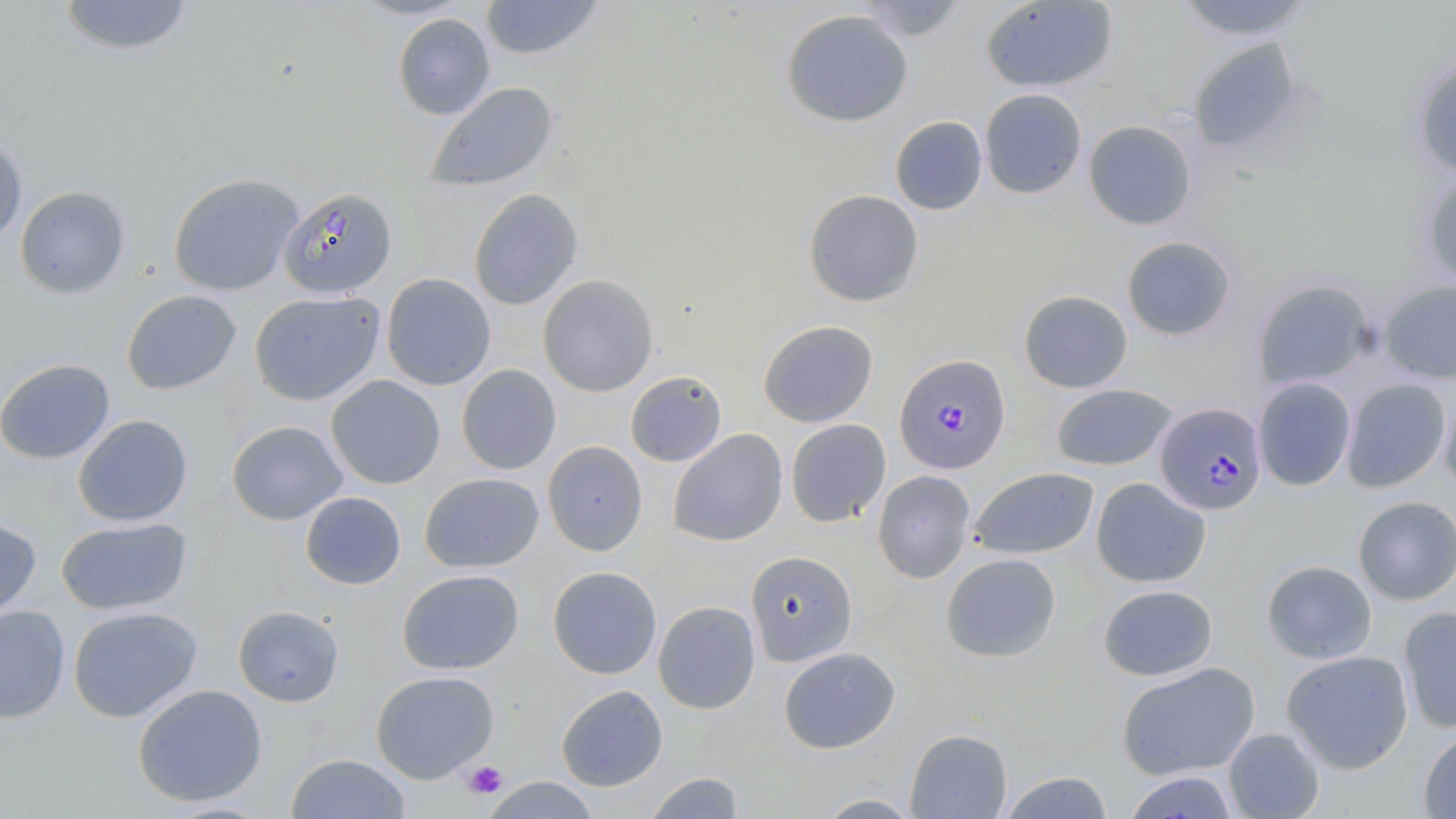

Approximate bounding boxes as named x1/y1/x2/y2 corners in pixels. Platelet locations: (x1=463, y1=760, x2=507, y2=798). Uninfected red blood cell locations: (x1=56, y1=0, x2=195, y2=57), (x1=479, y1=0, x2=606, y2=60), (x1=853, y1=0, x2=968, y2=42), (x1=1173, y1=0, x2=1314, y2=40), (x1=981, y1=1, x2=1118, y2=92), (x1=781, y1=9, x2=913, y2=127), (x1=392, y1=13, x2=495, y2=120), (x1=1188, y1=38, x2=1301, y2=153), (x1=1411, y1=59, x2=1456, y2=180), (x1=425, y1=82, x2=559, y2=192), (x1=979, y1=88, x2=1087, y2=199), (x1=889, y1=116, x2=987, y2=214), (x1=1083, y1=120, x2=1197, y2=230), (x1=0, y1=137, x2=27, y2=247), (x1=168, y1=173, x2=303, y2=296), (x1=1420, y1=174, x2=1456, y2=289), (x1=15, y1=185, x2=130, y2=298), (x1=468, y1=189, x2=583, y2=310), (x1=803, y1=189, x2=924, y2=306), (x1=1121, y1=235, x2=1237, y2=341), (x1=381, y1=273, x2=496, y2=391), (x1=538, y1=274, x2=658, y2=396), (x1=1252, y1=278, x2=1378, y2=391), (x1=1367, y1=279, x2=1454, y2=491), (x1=1378, y1=279, x2=1456, y2=384), (x1=121, y1=290, x2=242, y2=395), (x1=1019, y1=290, x2=1133, y2=393), (x1=249, y1=291, x2=385, y2=406), (x1=758, y1=320, x2=878, y2=427), (x1=0, y1=358, x2=115, y2=464), (x1=456, y1=364, x2=561, y2=474), (x1=625, y1=371, x2=727, y2=467), (x1=325, y1=375, x2=445, y2=489), (x1=1253, y1=377, x2=1356, y2=491), (x1=1341, y1=378, x2=1452, y2=492), (x1=1051, y1=383, x2=1177, y2=471), (x1=1439, y1=387, x2=1456, y2=497), (x1=73, y1=415, x2=193, y2=526), (x1=785, y1=419, x2=890, y2=528), (x1=226, y1=420, x2=348, y2=525), (x1=667, y1=429, x2=788, y2=546), (x1=542, y1=441, x2=648, y2=555), (x1=969, y1=467, x2=1099, y2=560), (x1=872, y1=470, x2=976, y2=583), (x1=419, y1=472, x2=544, y2=573), (x1=1091, y1=477, x2=1211, y2=588), (x1=300, y1=491, x2=406, y2=590), (x1=1353, y1=496, x2=1456, y2=605), (x1=0, y1=515, x2=41, y2=623), (x1=55, y1=517, x2=192, y2=616), (x1=745, y1=551, x2=858, y2=666), (x1=941, y1=553, x2=1060, y2=662), (x1=1262, y1=560, x2=1377, y2=664), (x1=547, y1=566, x2=662, y2=679), (x1=397, y1=569, x2=524, y2=675), (x1=1098, y1=584, x2=1218, y2=681), (x1=653, y1=601, x2=760, y2=714), (x1=0, y1=605, x2=71, y2=723), (x1=232, y1=605, x2=344, y2=707), (x1=68, y1=606, x2=202, y2=722), (x1=1398, y1=606, x2=1456, y2=733), (x1=778, y1=647, x2=901, y2=754), (x1=1281, y1=650, x2=1414, y2=773), (x1=1116, y1=662, x2=1260, y2=780), (x1=371, y1=671, x2=499, y2=783), (x1=132, y1=684, x2=267, y2=807), (x1=556, y1=685, x2=668, y2=791), (x1=1223, y1=727, x2=1325, y2=818), (x1=905, y1=728, x2=1012, y2=818), (x1=1418, y1=728, x2=1456, y2=818), (x1=285, y1=753, x2=411, y2=818), (x1=643, y1=771, x2=745, y2=818), (x1=999, y1=771, x2=1115, y2=818), (x1=1122, y1=771, x2=1239, y2=818), (x1=480, y1=777, x2=601, y2=818), (x1=814, y1=793, x2=924, y2=818). Plasmodium falciparum-infected red blood cell locations: (x1=279, y1=187, x2=397, y2=297), (x1=894, y1=353, x2=1011, y2=474), (x1=1154, y1=402, x2=1267, y2=515). Slide-level diagnosis: Plasmodium falciparum. Thin blood film. Single field of view. Captured at 1000x magnification. Image is 1456×819 pixels. May-Grünwald-Giemsa stain. Optical microscopy.